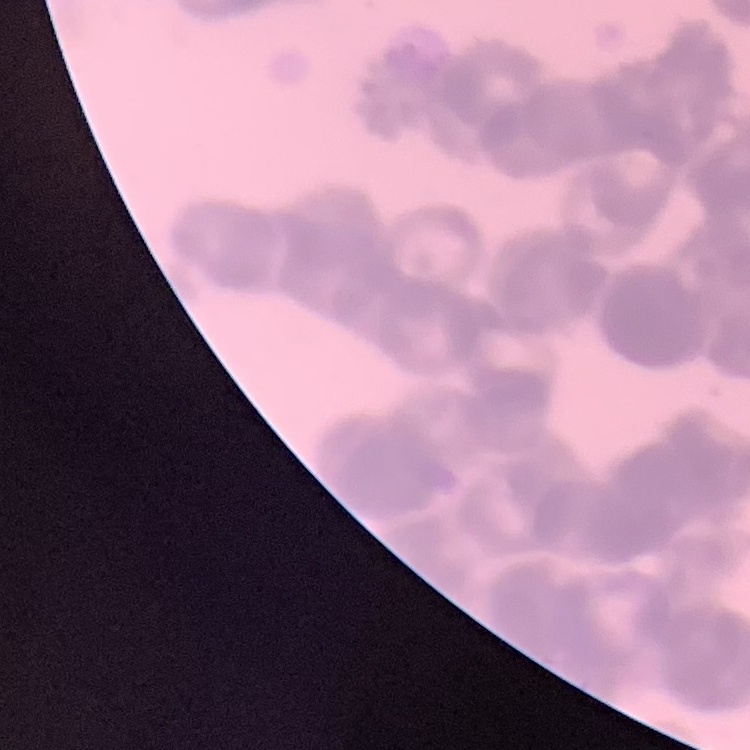

erythrocyte morphology = rouleaux formation
stain = Field's or Giemsa
image type = one tile cut from a larger photomicrograph
preparation = thin blood smear